Describe the morphology of the red blood cells.
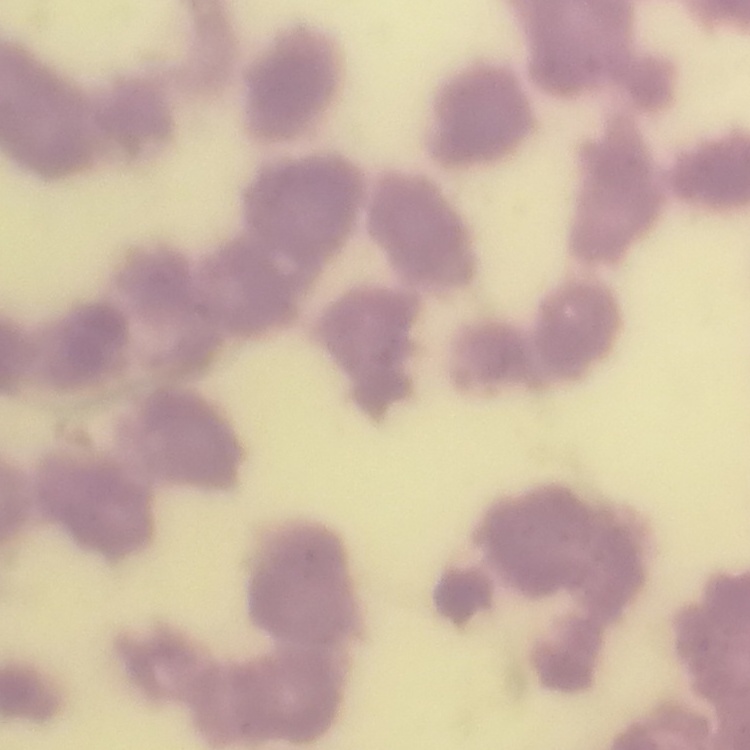
Rouleaux formation.

Summary:
  - Preparation: thin blood smear
  - Image type: one tile cut from a larger photomicrograph
  - Stain: Field's or Giemsa